State which parasite is depicted.
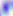
Toxoplasma gondii.

Micrograph. 400x magnification.